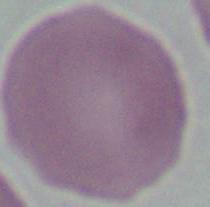
identification = red blood cell
magnification = 1000x
modality = micrograph